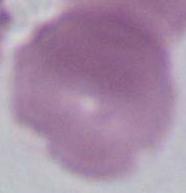

Summary:
  - Modality: photomicrograph
  - Identification: red blood cell
  - Magnification: 1000x